Report the malaria status of this cell.
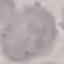

It is uninfected.

preparation = thin smear
stain = Giemsa
capture = smartphone through the microscope eyepiece
image type = cell patch, automatically extracted from a larger field of view and resized to 64 × 64 pixels